Locate every Plasmodium falciparum-infected red blood cell.
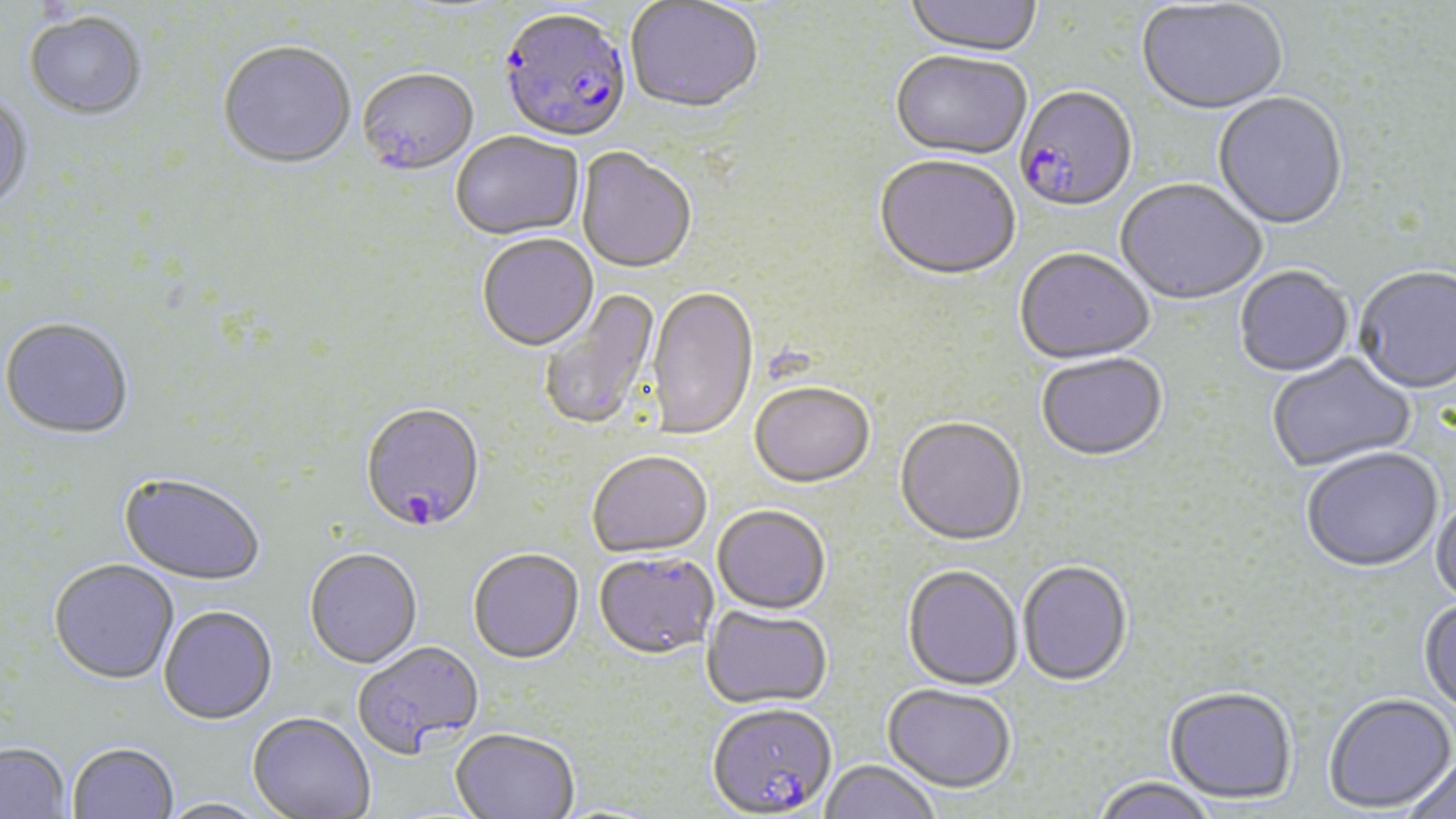
Approximate bounding boxes as (x1,y1)-(x2,y2) corner pairs in pixels.
Plasmodium falciparum-infected red blood cells (subset): (500,12)-(632,146), (360,406)-(486,535), (707,703)-(837,818).

Uninfected red blood cell locations (subset): (905,0)-(1042,60), (1136,1)-(1288,117), (625,2)-(763,117), (23,13)-(147,123), (218,45)-(356,172), (890,53)-(1030,162), (358,71)-(479,179), (1213,93)-(1348,232), (0,95)-(34,215), (451,133)-(584,243), (576,149)-(696,276), (874,158)-(1020,284), (1115,180)-(1267,307), (477,235)-(599,354), (1015,250)-(1154,367), (1234,268)-(1353,379), (1354,269)-(1456,397), (539,287)-(662,430), (646,287)-(759,442), (0,318)-(135,442), (1267,353)-(1417,474), (1036,356)-(1168,463), (749,384)-(875,490), (894,418)-(1027,548), (1301,449)-(1444,575), (587,452)-(713,560), (118,475)-(265,588), (1431,495)-(1456,610), (713,506)-(831,616), (304,550)-(423,670), (468,550)-(584,666), (594,552)-(719,661), (48,561)-(180,687), (1017,562)-(1133,688), (902,565)-(1023,691), (1418,598)-(1456,721), (702,606)-(832,710), (159,608)-(279,727), (352,643)-(484,760), (882,683)-(1016,793), (1165,686)-(1298,804), (1322,693)-(1456,813), (247,714)-(375,819), (450,728)-(579,818), (0,743)-(71,819), (67,744)-(178,819), (1403,753)-(1456,819), (820,759)-(942,819), (1091,776)-(1219,819), (158,798)-(273,819). Slide-level diagnosis: Plasmodium falciparum. 1000x magnification. Image is 1456×819 pixels. May-Grünwald-Giemsa-stained preparation. One field of a larger specimen. Light microscopy. Thin blood smear.